Locate every Plasmodium malariae-infected red blood cell.
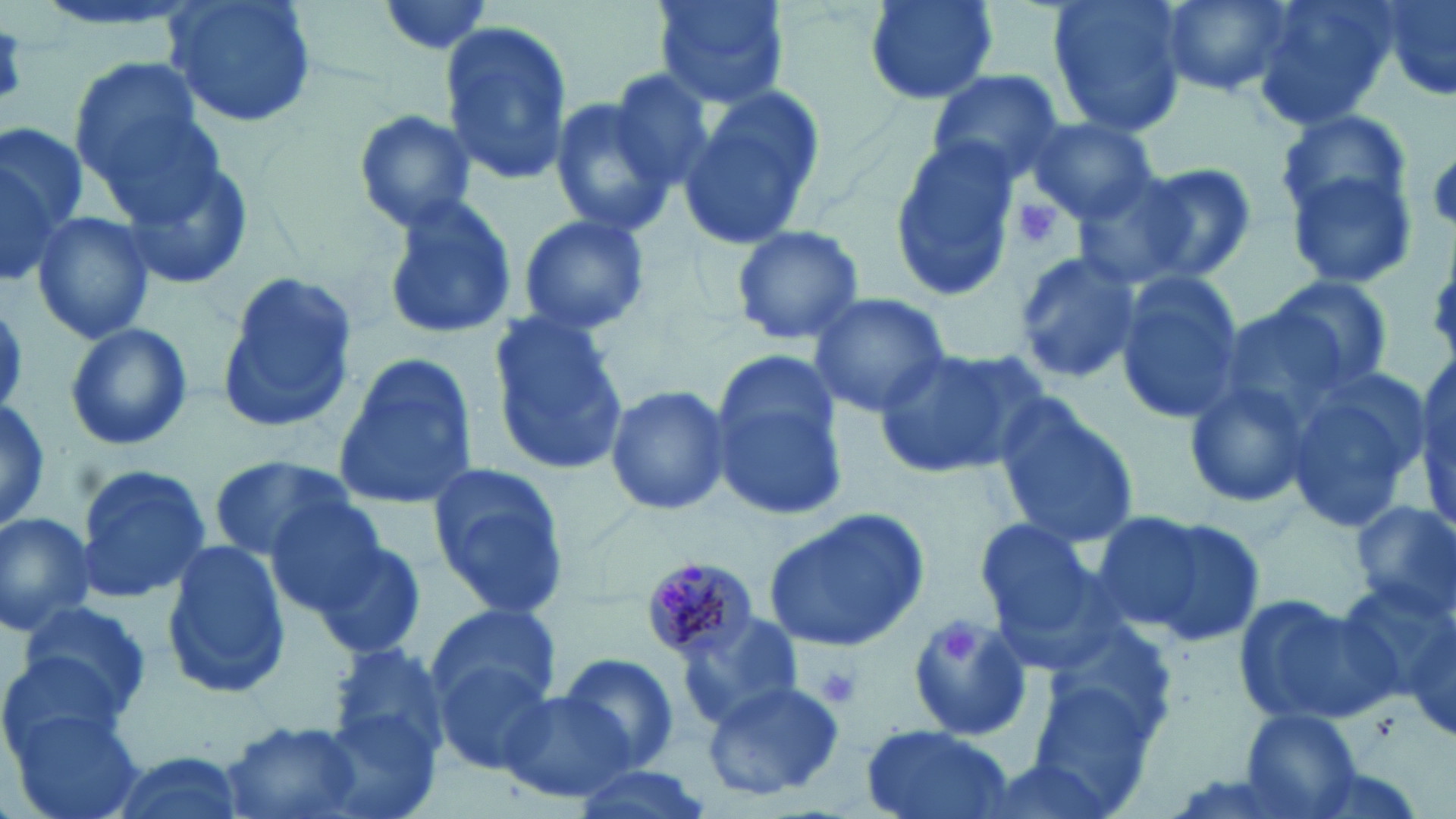
Approximate bounding boxes as named x1/y1/x2/y2 corners in pixels.
Plasmodium malariae-infected red blood cells: (x1=645, y1=558, x2=756, y2=663).

{
  "slide_level_diagnosis": "Plasmodium malariae",
  "preparation": "thin blood film",
  "stain": "May-Grünwald-Giemsa",
  "field_of_view": "single",
  "magnification": "1000x",
  "platelet_locations": "approximate bounding boxes as named x1/y1/x2/y2 corners in pixels: (x1=1428, y1=151, x2=1456, y2=231), (x1=1008, y1=194, x2=1067, y2=253), (x1=943, y1=625, x2=983, y2=666), (x1=816, y1=665, x2=863, y2=710)",
  "uninfected_red_blood_cell_locations": "approximate bounding boxes as named x1/y1/x2/y2 corners in pixels: (x1=161, y1=0, x2=319, y2=130), (x1=375, y1=0, x2=500, y2=59), (x1=654, y1=0, x2=789, y2=108), (x1=860, y1=0, x2=1003, y2=104), (x1=1047, y1=0, x2=1189, y2=135), (x1=1154, y1=0, x2=1297, y2=99), (x1=1254, y1=0, x2=1395, y2=132), (x1=1378, y1=0, x2=1456, y2=105), (x1=439, y1=18, x2=572, y2=187), (x1=67, y1=59, x2=215, y2=199), (x1=603, y1=66, x2=729, y2=195), (x1=924, y1=68, x2=1066, y2=189), (x1=680, y1=91, x2=822, y2=251), (x1=547, y1=96, x2=676, y2=236), (x1=1275, y1=107, x2=1417, y2=236), (x1=352, y1=108, x2=479, y2=229), (x1=1026, y1=116, x2=1159, y2=225), (x1=0, y1=121, x2=89, y2=239), (x1=890, y1=141, x2=1021, y2=299), (x1=113, y1=153, x2=256, y2=292), (x1=0, y1=155, x2=66, y2=287), (x1=1115, y1=162, x2=1258, y2=286), (x1=1284, y1=166, x2=1418, y2=292), (x1=1071, y1=176, x2=1204, y2=289), (x1=380, y1=194, x2=519, y2=343), (x1=32, y1=209, x2=156, y2=347), (x1=515, y1=213, x2=652, y2=339), (x1=730, y1=223, x2=866, y2=347), (x1=1014, y1=248, x2=1140, y2=383), (x1=216, y1=269, x2=357, y2=433), (x1=1113, y1=273, x2=1244, y2=428), (x1=1265, y1=274, x2=1394, y2=392), (x1=805, y1=294, x2=954, y2=418), (x1=0, y1=302, x2=31, y2=410), (x1=487, y1=314, x2=629, y2=477), (x1=64, y1=322, x2=194, y2=452), (x1=874, y1=345, x2=1043, y2=479), (x1=708, y1=351, x2=846, y2=520), (x1=332, y1=352, x2=478, y2=512), (x1=1278, y1=362, x2=1430, y2=533), (x1=1184, y1=373, x2=1317, y2=510), (x1=604, y1=387, x2=731, y2=516), (x1=988, y1=396, x2=1139, y2=550), (x1=0, y1=399, x2=52, y2=529), (x1=206, y1=455, x2=353, y2=563), (x1=72, y1=462, x2=214, y2=604), (x1=427, y1=464, x2=571, y2=620), (x1=263, y1=495, x2=391, y2=618), (x1=1351, y1=500, x2=1455, y2=619), (x1=764, y1=508, x2=931, y2=654), (x1=0, y1=511, x2=100, y2=639), (x1=1108, y1=513, x2=1268, y2=646), (x1=973, y1=515, x2=1103, y2=646), (x1=310, y1=537, x2=428, y2=661), (x1=158, y1=538, x2=293, y2=698), (x1=1347, y1=576, x2=1456, y2=716), (x1=1231, y1=592, x2=1402, y2=725), (x1=15, y1=598, x2=152, y2=720), (x1=428, y1=603, x2=562, y2=717), (x1=908, y1=610, x2=1034, y2=743), (x1=673, y1=614, x2=805, y2=733), (x1=328, y1=646, x2=449, y2=765), (x1=0, y1=652, x2=128, y2=764), (x1=432, y1=652, x2=561, y2=775), (x1=556, y1=654, x2=682, y2=774), (x1=1020, y1=678, x2=1164, y2=815), (x1=700, y1=680, x2=846, y2=803), (x1=499, y1=688, x2=637, y2=802), (x1=8, y1=707, x2=146, y2=819), (x1=1241, y1=709, x2=1361, y2=817), (x1=220, y1=720, x2=365, y2=819), (x1=860, y1=724, x2=1016, y2=819), (x1=100, y1=750, x2=247, y2=819), (x1=970, y1=754, x2=1123, y2=819), (x1=568, y1=763, x2=717, y2=819)",
  "image_size": "1456×819 pixels",
  "modality": "light microscopy"
}